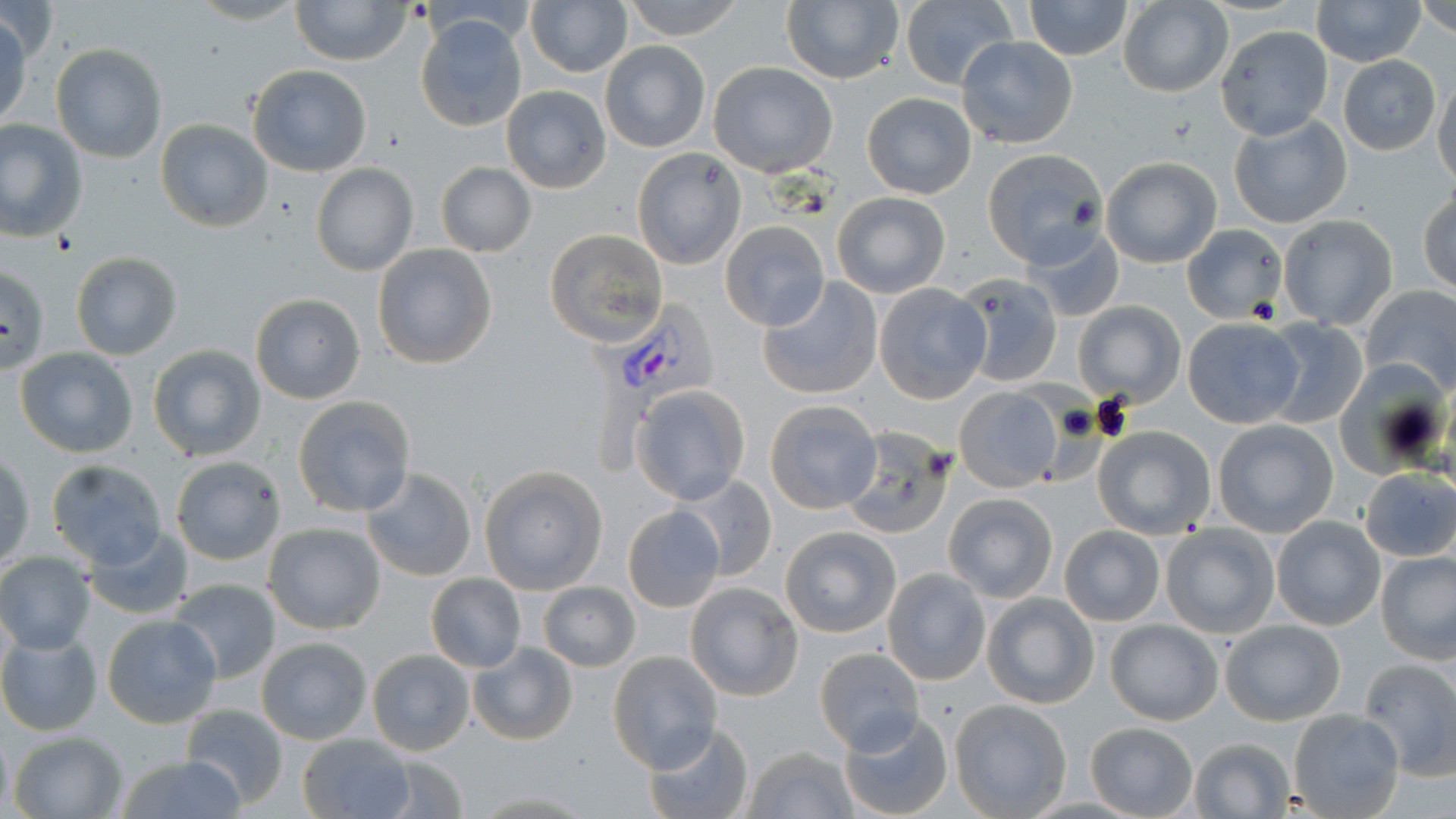

Summary:
  - Coordinate format: approximate bounding boxes as [x1, y1, x2, y2] in pixels
  - Plasmodium vivax-infected red blood cell locations: [582, 303, 717, 470]
  - Uninfected red blood cell locations: [185, 0, 310, 27], [290, 0, 412, 66], [621, 0, 746, 41], [782, 0, 905, 87], [900, 0, 1018, 91], [1022, 0, 1132, 60], [1311, 0, 1426, 67], [525, 1, 632, 78], [1415, 1, 1456, 38], [1117, 2, 1234, 97], [0, 12, 31, 132], [413, 12, 529, 134], [1214, 23, 1335, 139], [955, 36, 1079, 151], [599, 40, 710, 153], [50, 43, 168, 164], [1337, 56, 1441, 154], [708, 62, 839, 178], [247, 63, 373, 177], [1432, 76, 1456, 192], [500, 85, 611, 194], [862, 92, 976, 200], [1228, 113, 1353, 230], [0, 119, 88, 241], [155, 119, 273, 232], [631, 146, 746, 269], [981, 148, 1108, 266], [1100, 157, 1222, 268], [436, 162, 537, 258], [311, 164, 419, 278], [1418, 189, 1456, 297], [832, 192, 950, 297], [1278, 213, 1397, 330], [719, 220, 831, 332], [1020, 223, 1124, 324], [1181, 223, 1288, 322], [544, 229, 667, 346], [371, 243, 498, 370], [71, 251, 182, 360], [0, 264, 50, 375], [951, 272, 1064, 386], [757, 275, 883, 400], [874, 283, 991, 404], [1359, 285, 1456, 397], [248, 292, 367, 405], [1073, 303, 1185, 404], [1182, 316, 1304, 428], [1260, 318, 1370, 428], [147, 344, 268, 462], [15, 346, 139, 457], [953, 383, 1067, 491], [630, 384, 752, 505], [292, 395, 418, 518], [764, 398, 884, 514], [1212, 418, 1339, 537], [1092, 425, 1218, 540], [839, 427, 955, 539], [1, 451, 35, 570], [171, 455, 285, 565], [45, 458, 170, 570], [478, 466, 608, 594], [360, 467, 477, 582], [1358, 469, 1456, 562], [673, 474, 777, 582], [942, 491, 1059, 602], [622, 504, 724, 611], [1271, 516, 1386, 632], [263, 522, 386, 634], [1159, 522, 1282, 639], [83, 524, 195, 620], [1059, 525, 1165, 626], [780, 526, 901, 637], [1376, 549, 1456, 663], [0, 552, 96, 654], [882, 569, 991, 685], [425, 574, 526, 672], [169, 579, 283, 685], [685, 582, 802, 702], [538, 583, 640, 671], [981, 593, 1100, 710], [101, 614, 223, 730], [1219, 618, 1345, 726], [1105, 619, 1224, 725], [0, 628, 102, 736], [256, 636, 373, 745], [468, 642, 578, 745], [367, 648, 475, 755], [811, 648, 927, 755], [609, 651, 721, 772], [1358, 657, 1456, 779], [948, 698, 1071, 818], [180, 703, 289, 810], [1287, 708, 1406, 819], [837, 709, 954, 819], [642, 720, 754, 819], [1084, 721, 1198, 817], [8, 731, 127, 818], [297, 733, 415, 818], [1187, 737, 1297, 818], [741, 745, 860, 818], [114, 751, 246, 819], [369, 752, 467, 818], [465, 787, 598, 816]
  - Slide-level diagnosis: Plasmodium vivax
  - Field of view: one of a larger specimen
  - Magnification: 1000x
  - Modality: optical microscopy
  - Image size: 1456×819 pixels
  - Stain: May-Grünwald-Giemsa
  - Preparation: thin blood smear